Name the parasite shown.
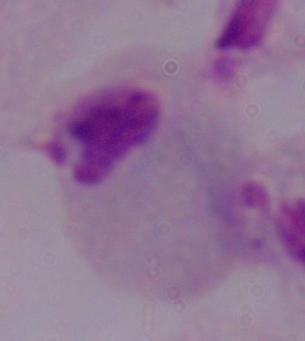

This is a trichomonad.

Photomicrograph. Captured at 1000x magnification.